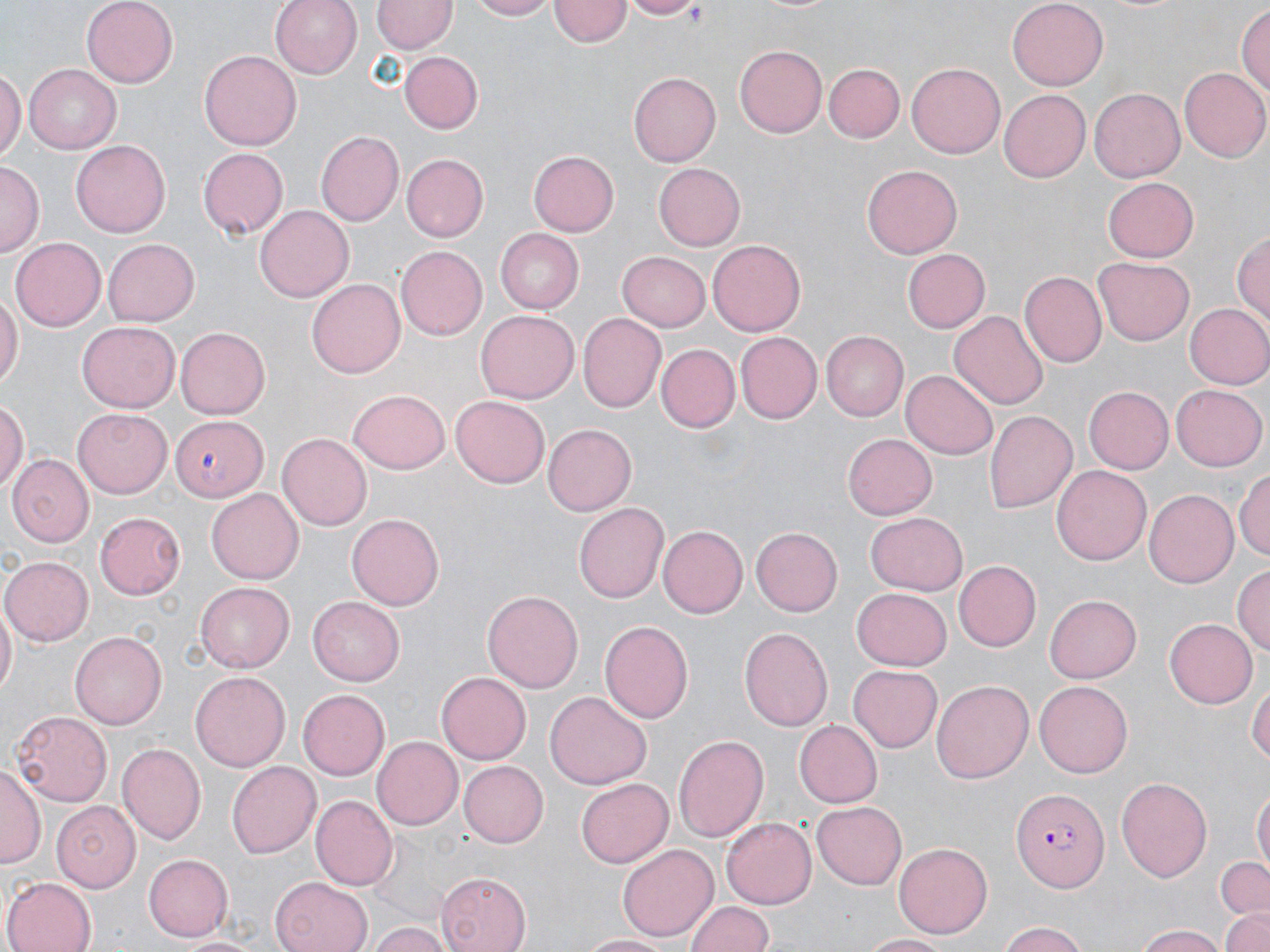

Approximate bounding boxes as (x1,y1)-(x2,y2) corner pairs in pixels. Uninfected red blood cell locations: (82,0)-(179,88), (268,0)-(363,80), (469,0)-(558,20), (619,0)-(703,19), (1008,0)-(1107,87), (372,1)-(455,54), (551,1)-(632,49), (1236,4)-(1270,100), (734,45)-(828,137), (199,49)-(302,149), (402,52)-(482,133), (822,63)-(905,142), (906,63)-(1006,160), (0,65)-(25,163), (24,65)-(120,153), (1180,69)-(1268,163), (628,72)-(719,167), (1088,87)-(1185,182), (998,89)-(1092,182), (315,131)-(402,227), (71,138)-(169,233), (198,148)-(289,239), (528,151)-(620,236), (400,153)-(487,241), (0,162)-(42,254), (654,164)-(746,249), (863,164)-(963,259), (1103,176)-(1197,262), (256,203)-(355,303), (497,229)-(584,313), (1234,229)-(1268,334), (10,236)-(104,327), (103,237)-(199,324), (707,238)-(804,334), (396,245)-(489,339), (902,248)-(990,333), (617,251)-(711,331), (1093,257)-(1195,345), (1020,271)-(1107,367), (307,278)-(405,379), (0,291)-(21,395), (1184,302)-(1270,390), (475,309)-(578,404), (949,310)-(1049,410), (579,312)-(667,413), (76,322)-(180,413), (176,326)-(274,418), (820,331)-(907,420), (736,332)-(822,422), (657,343)-(741,432), (900,368)-(997,458), (1084,386)-(1174,474), (1170,386)-(1265,471), (349,390)-(452,473), (451,393)-(549,485), (0,399)-(27,498), (73,409)-(171,497), (985,409)-(1077,514), (168,416)-(264,501), (545,423)-(638,517), (277,433)-(372,530), (843,434)-(938,522), (11,453)-(95,546), (1052,465)-(1151,566), (1233,466)-(1270,565), (208,488)-(303,584), (1144,489)-(1239,588), (575,502)-(669,603), (96,512)-(186,598), (348,512)-(445,610), (866,512)-(966,594), (659,524)-(747,618), (750,526)-(843,616), (1,556)-(93,645), (954,561)-(1040,651), (1233,564)-(1269,660), (194,581)-(295,673), (853,588)-(952,672), (483,589)-(583,694), (0,595)-(16,702), (308,596)-(403,685), (1046,596)-(1141,683), (599,618)-(694,726), (1165,618)-(1257,709), (739,626)-(833,733), (70,628)-(165,727), (848,665)-(942,752), (191,670)-(289,771), (437,671)-(532,764), (931,678)-(1033,784), (1249,678)-(1269,775), (1034,680)-(1133,777), (298,689)-(389,778), (544,692)-(650,790), (10,711)-(112,806), (795,720)-(883,808), (672,732)-(770,843), (372,736)-(463,831), (118,743)-(206,845), (227,761)-(322,859), (457,761)-(549,847), (1,762)-(42,870), (1116,777)-(1212,881), (576,779)-(674,869), (1252,787)-(1269,880), (312,795)-(398,888), (53,801)-(140,893), (811,803)-(907,891), (721,817)-(816,910), (894,842)-(993,937), (618,843)-(719,939), (141,852)-(232,942), (1214,857)-(1270,918), (437,872)-(530,952), (271,875)-(372,952), (4,876)-(98,952), (686,897)-(776,951), (1218,906)-(1270,952), (369,922)-(450,952), (996,924)-(1091,952), (1135,925)-(1230,952), (577,932)-(676,951), (860,932)-(949,952), (174,934)-(261,952). Plasmodium falciparum-infected red blood cell locations: (1010,783)-(1107,891). Slide-level diagnosis: Plasmodium falciparum. Thin blood film. Optical microscopy. Captured at 1000x magnification. One field of a larger specimen. May-Grünwald-Giemsa-stained preparation. Image is 1270×952 pixels.